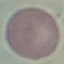 Malaria status: uninfected. Giemsa stain. Thin smear of blood. Cell patch, automatically extracted from a larger field of view and resized to 64 × 64 pixels. Photographed with a smartphone camera at the microscope eyepiece.